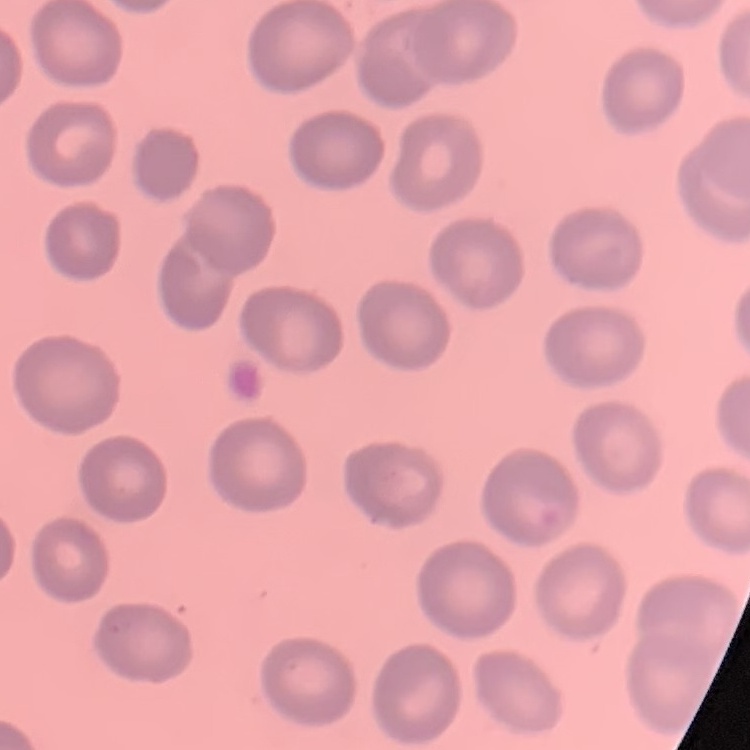

erythrocyte morphology = no rouleaux formation
preparation = thin blood film
image type = square crop of a larger photomicrograph
stain = Field's or Giemsa